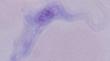
Summary:
  - Identification: trypanosome
  - Modality: photomicrograph
  - Magnification: 1000x